Name the parasite shown.
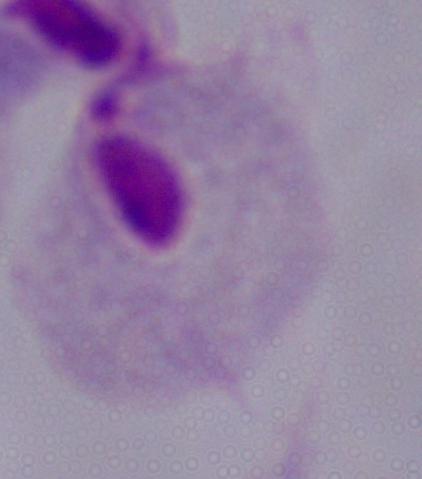

A trichomonad.

{
  "magnification": "1000x",
  "modality": "photomicrograph"
}